Locate every uninfected red blood cell.
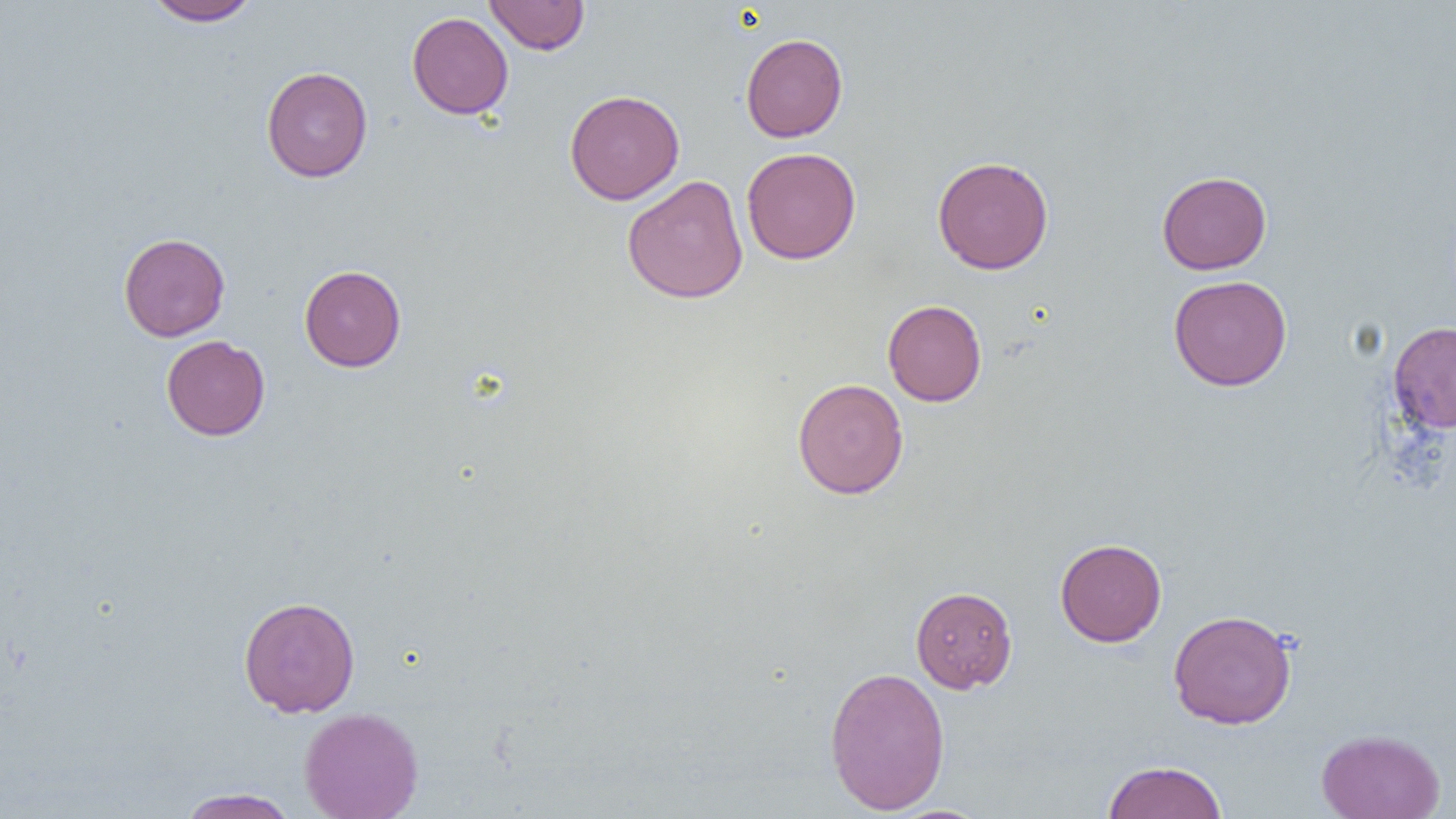

Approximate bounding boxes as named x1/y1/x2/y2 corners in pixels.
Uninfected red blood cells: (x1=145, y1=0, x2=261, y2=26), (x1=484, y1=0, x2=590, y2=55), (x1=407, y1=12, x2=513, y2=119), (x1=741, y1=33, x2=848, y2=142), (x1=261, y1=66, x2=373, y2=182), (x1=564, y1=89, x2=685, y2=204), (x1=742, y1=147, x2=861, y2=264), (x1=932, y1=156, x2=1053, y2=274), (x1=1156, y1=170, x2=1272, y2=275), (x1=622, y1=175, x2=749, y2=304), (x1=118, y1=232, x2=230, y2=342), (x1=299, y1=265, x2=406, y2=372), (x1=1168, y1=275, x2=1293, y2=391), (x1=883, y1=299, x2=987, y2=406), (x1=1388, y1=321, x2=1456, y2=434), (x1=161, y1=335, x2=270, y2=440), (x1=792, y1=378, x2=908, y2=499), (x1=1054, y1=537, x2=1167, y2=646), (x1=910, y1=586, x2=1017, y2=693), (x1=238, y1=595, x2=361, y2=718), (x1=1168, y1=609, x2=1297, y2=729), (x1=824, y1=666, x2=951, y2=815), (x1=299, y1=707, x2=424, y2=818), (x1=1316, y1=729, x2=1445, y2=819), (x1=1102, y1=760, x2=1228, y2=819), (x1=177, y1=787, x2=299, y2=818).

Slide-level diagnosis: no evidence of blood parasites. One field of a larger specimen. Image is 1456×819 pixels. 1000x magnification. Thin blood smear. Light microscopy.